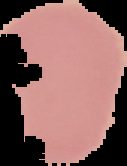 The area outside the segmented cell region is set to black. From a thin blood film. Malaria status: uninfected. Image is 127×166 pixels.